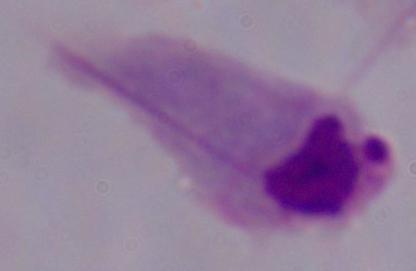 Micrograph. A trichomonad is shown. Captured at 1000x magnification.